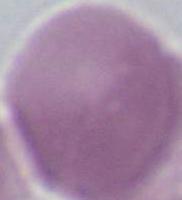
1000x magnification. Photomicrograph. An erythrocyte is seen.